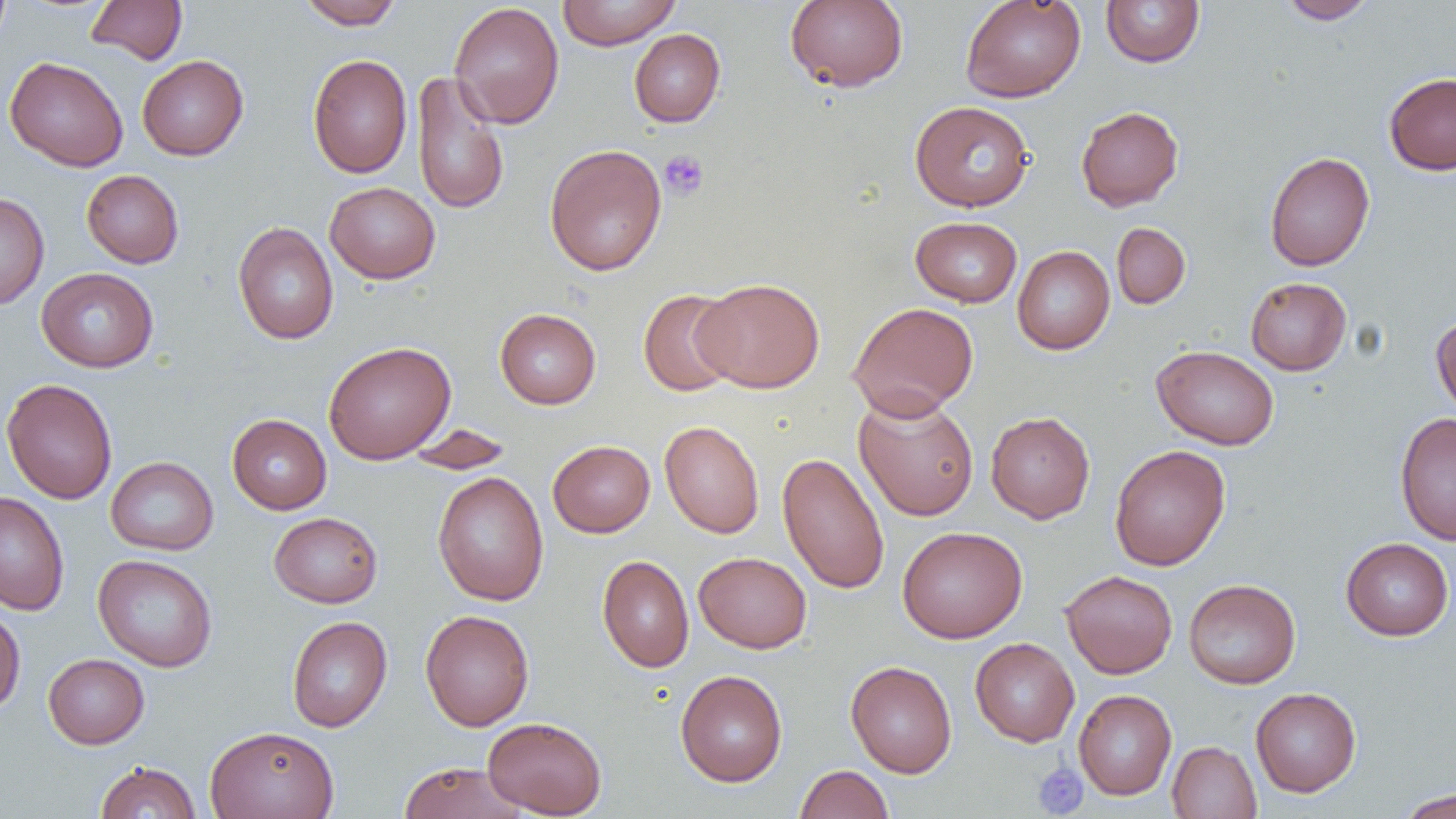

slide_level_diagnosis: no evidence of blood parasites
platelet_locations: 'approximate bounding boxes as (x1,y1)-(x2,y2) corner pairs in pixels: (659,149)-(709,200), (1032,761)-(1088,818)'
image_size: 1456×819 pixels
uninfected_red_blood_cell_locations: 'approximate bounding boxes as (x1,y1)-(x2,y2) corner pairs in pixels: (86,0)-(187,65), (296,0)-(404,29), (557,0)-(681,50), (785,0)-(908,92), (960,0)-(1086,103), (1100,0)-(1205,68), (1278,0)-(1379,24), (449,2)-(565,129), (629,29)-(725,127), (307,54)-(412,178), (137,55)-(249,160), (4,56)-(129,172), (411,71)-(509,216), (1384,72)-(1456,175), (910,101)-(1035,212), (1076,106)-(1184,211), (544,143)-(667,276), (1264,151)-(1375,271), (81,170)-(184,268), (324,182)-(440,284), (0,192)-(50,309), (910,216)-(1022,307), (232,222)-(338,345), (1111,222)-(1190,309), (1012,246)-(1115,355), (36,267)-(159,372), (1245,277)-(1351,375), (695,278)-(824,393), (638,288)-(742,396), (848,301)-(979,419), (495,308)-(601,409), (1431,314)-(1456,421), (323,341)-(456,464), (1151,344)-(1280,450), (1,378)-(118,504), (853,392)-(979,521), (985,411)-(1095,523), (1394,413)-(1456,544), (227,414)-(332,514), (660,420)-(765,538), (402,423)-(515,475), (547,440)-(655,537), (1109,444)-(1231,571), (777,452)-(890,595), (105,456)-(218,555), (432,471)-(549,606), (0,491)-(70,615), (269,511)-(383,608), (897,526)-(1027,643), (1340,537)-(1454,640), (694,551)-(812,653), (93,554)-(218,672), (597,554)-(694,672), (1060,569)-(1178,678), (1183,579)-(1301,689), (0,606)-(26,715), (420,609)-(534,731), (287,616)-(392,732), (970,638)-(1079,746), (43,653)-(149,749), (845,660)-(957,777), (675,669)-(787,787), (1250,687)-(1361,797), (1074,689)-(1176,800), (483,716)-(607,817), (204,725)-(339,819), (1167,741)-(1261,819), (94,761)-(201,818), (398,761)-(528,819), (794,764)-(893,819), (1396,787)-(1456,818)'
field_of_view: one of a larger specimen
magnification: 1000x
modality: light microscopy
preparation: thin blood film